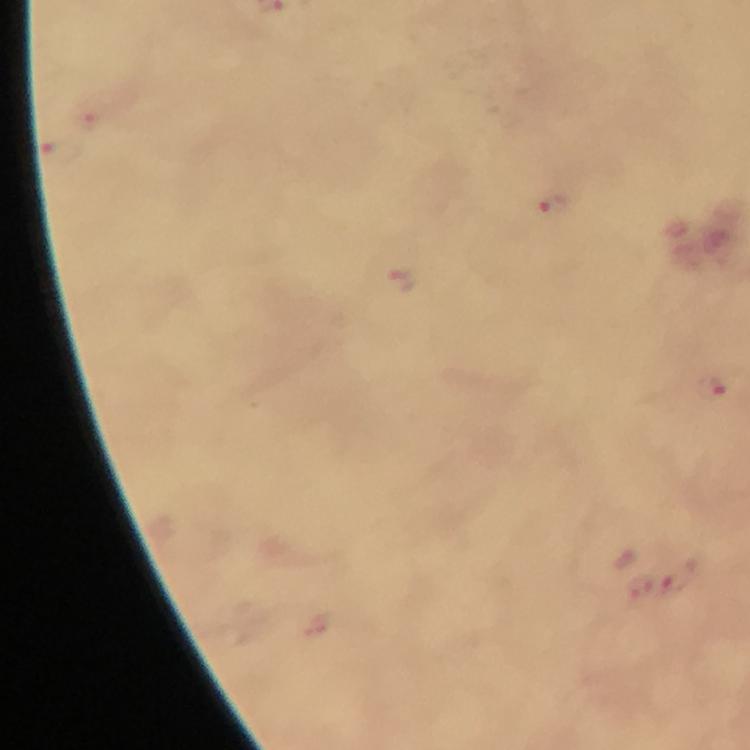
{
  "capture": "smartphone camera through the microscope",
  "image_size": "750×750 pixels",
  "stain": "Giemsa",
  "malaria_parasite_locations": "approximate centers as (x, y) in pixels: (552, 205), (403, 279), (711, 386), (676, 575)",
  "cropped_from": "a single field of view",
  "preparation": "thick blood smear",
  "immersion_oil": "applied",
  "magnification": "100x",
  "context": "from a diagnostic examination for malaria"
}